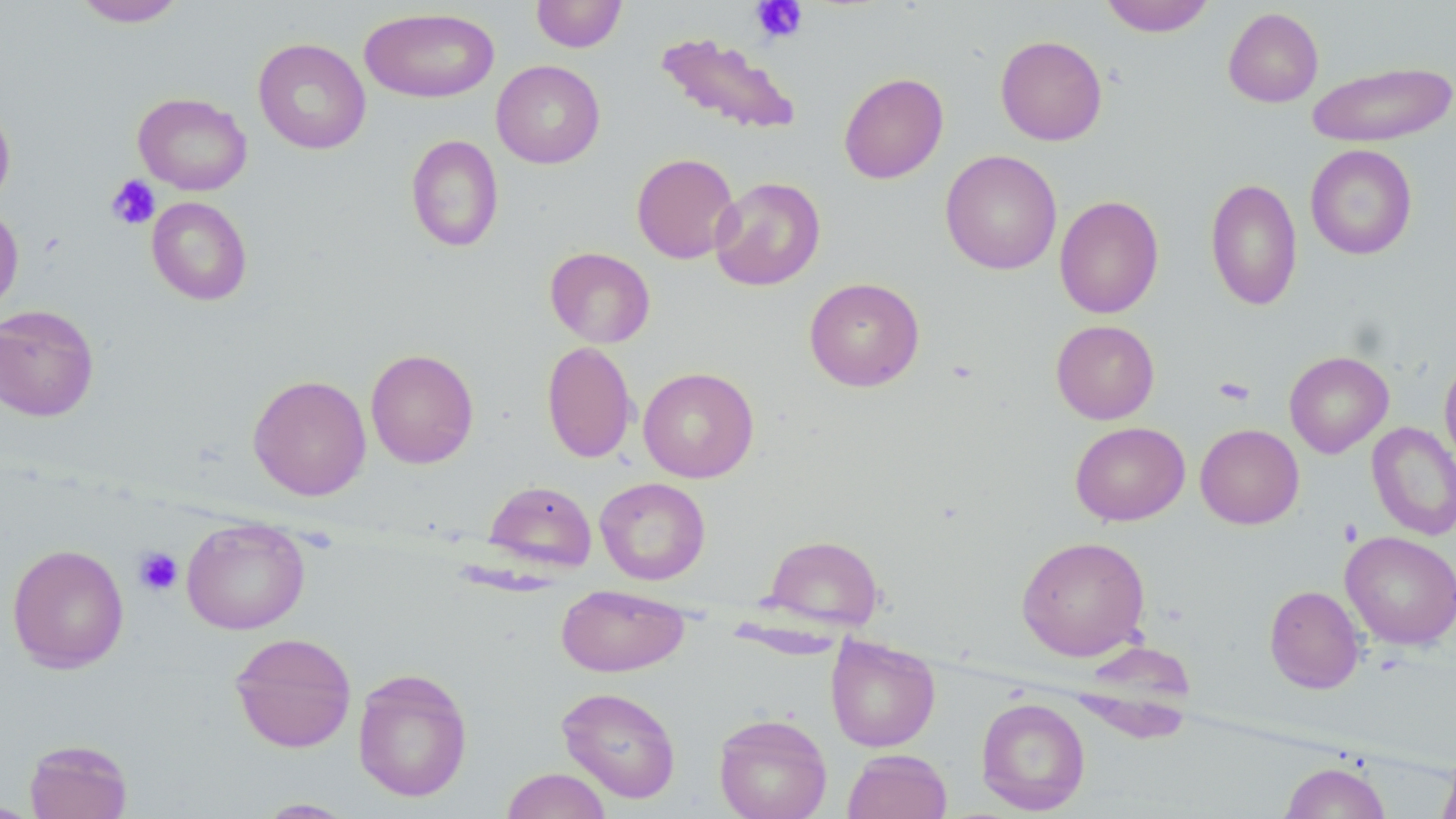
Summary:
  - Coordinate format: approximate bounding boxes as (x1, y1, x2, y2) in pixels
  - Platelet locations: (751, 0, 808, 43), (106, 175, 160, 230), (1213, 376, 1255, 406), (134, 547, 183, 596)
  - Uninfected red blood cell locations: (72, 0, 187, 27), (530, 0, 627, 53), (1100, 0, 1215, 37), (360, 7, 500, 103), (1223, 7, 1323, 107), (655, 32, 802, 135), (995, 35, 1107, 145), (253, 37, 371, 155), (491, 60, 605, 168), (1307, 61, 1455, 147), (838, 72, 949, 184), (133, 92, 253, 196), (0, 102, 16, 209), (406, 134, 504, 252), (1305, 144, 1417, 260), (940, 149, 1062, 275), (631, 152, 740, 264), (1205, 176, 1303, 311), (710, 177, 825, 291), (1054, 195, 1164, 318), (146, 196, 252, 306), (0, 203, 23, 319), (545, 247, 655, 348), (804, 277, 925, 392), (0, 304, 100, 422), (1051, 319, 1160, 424), (542, 340, 637, 464), (365, 348, 479, 469), (1284, 351, 1394, 458), (1439, 356, 1456, 471), (639, 367, 759, 483), (248, 374, 371, 501), (1070, 421, 1190, 526), (1367, 421, 1456, 541), (1195, 424, 1304, 529), (595, 476, 710, 585), (483, 480, 597, 573), (182, 517, 310, 634), (1340, 531, 1456, 650), (764, 534, 883, 632), (1016, 536, 1151, 661), (7, 543, 129, 673), (555, 584, 689, 677), (1264, 585, 1365, 694), (230, 631, 357, 752), (826, 636, 940, 752), (1072, 647, 1197, 743), (352, 667, 473, 802), (556, 686, 681, 803), (975, 697, 1091, 815), (713, 713, 832, 819), (24, 739, 133, 818), (843, 749, 952, 819), (1438, 752, 1456, 819), (1279, 760, 1392, 819), (501, 767, 613, 819), (252, 798, 359, 817), (0, 799, 46, 818)
  - Slide-level diagnosis: negative for blood parasites
  - Field of view: single
  - Image size: 1456×819 pixels
  - Stain: May-Grünwald-Giemsa
  - Preparation: thin blood smear
  - Magnification: 1000x
  - Modality: light microscopy